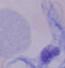

{
  "magnification": "1000x",
  "modality": "micrograph",
  "identification": "trypanosome"
}